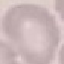
result: no malaria parasites seen
image_type: cell patch, automatically extracted from a larger field of view and resized to 64 × 64 pixels
preparation: thin smear
capture: smartphone through the microscope eyepiece
stain: Giemsa